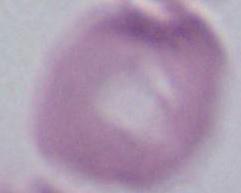
magnification = 1000x
modality = micrograph
identification = erythrocyte